Name the parasite shown.
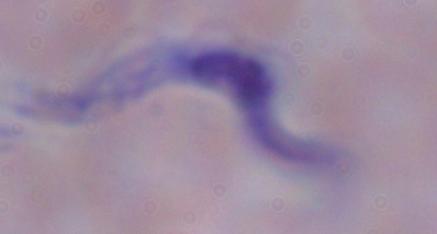

This is a trypanosome.

modality = micrograph
magnification = 1000x